Assess this cell for malaria.
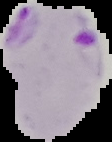
Parasitized.

From a thin blood smear. Cell region segmented out of the field of view; the surrounding area is masked to black. Image is 112×142 pixels.